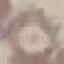
Summary:
  - Malaria status: uninfected
  - Stain: Giemsa
  - Preparation: thin smear
  - Capture: smartphone camera at the microscope eyepiece
  - Image type: cell patch, automatically extracted from a larger field of view and resized to 64 × 64 pixels